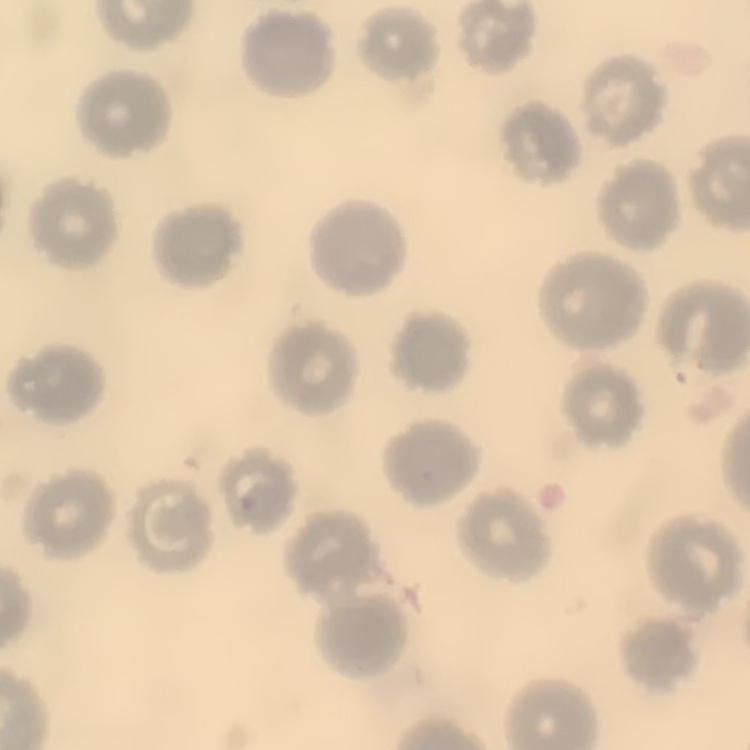

red blood cell morphology = no rouleaux formation
image type = one tile cut from a larger photomicrograph
stain = Field's or Giemsa
preparation = thin blood smear